Classify this cell by malaria status.
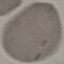

Uninfected.

Summary:
  - Capture: smartphone camera at the microscope eyepiece
  - Image type: cell patch, automatically extracted from a larger field of view and resized to 64 × 64 pixels
  - Stain: Giemsa
  - Preparation: thin smear